Draw a bounding box around every leukocyte (white blood cell).
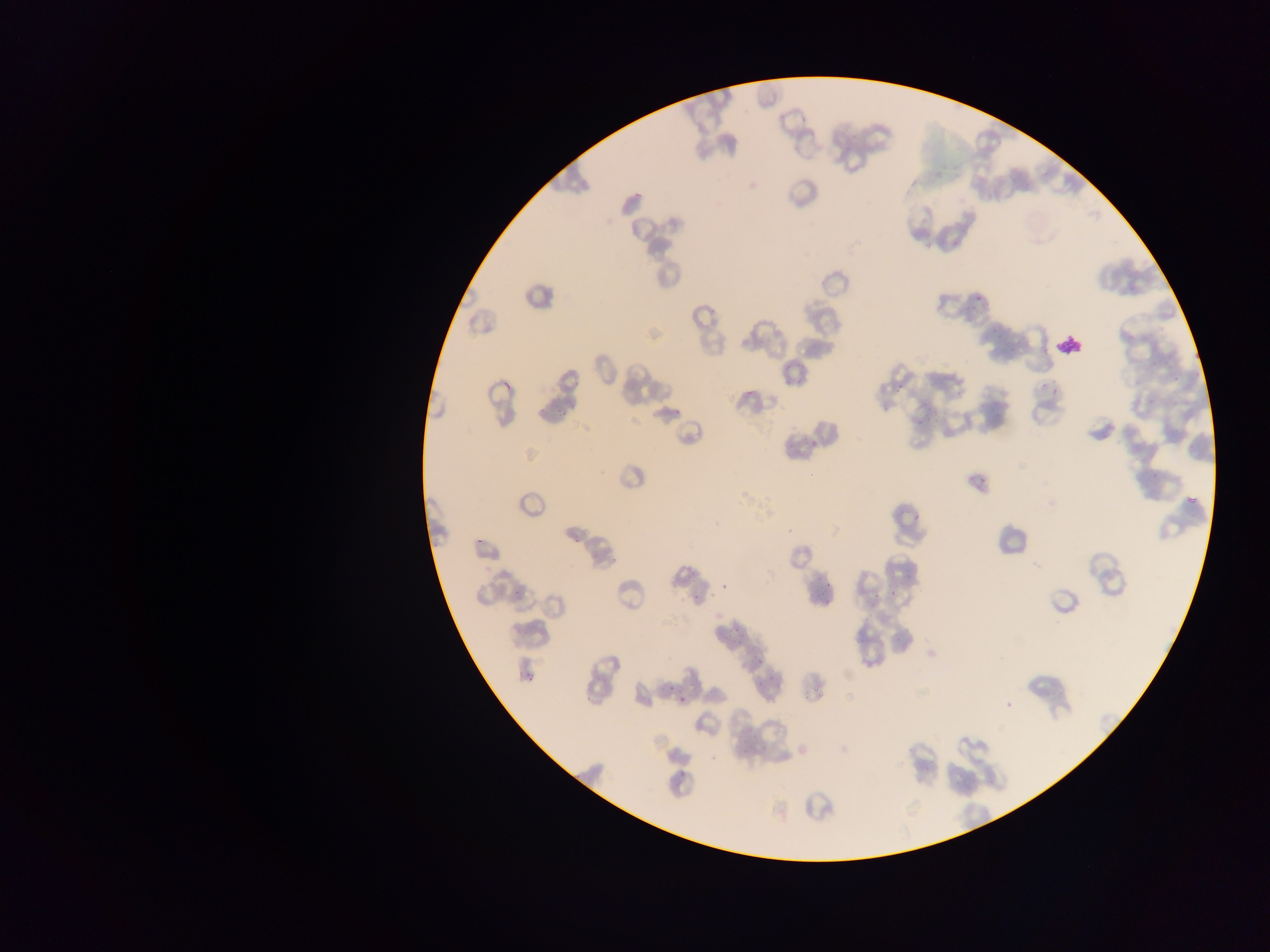
No leukocytes observed.

Approximate bounding boxes as (left, top, right, bottom) in pixels.
Summary:
  - Artifact (stain precipitate or debris) locations: (1058, 327, 1091, 359)
  - Plasmodium parasite locations: (630, 187, 648, 200), (963, 295, 982, 315), (992, 322, 1005, 335), (1043, 336, 1052, 355), (783, 373, 798, 388), (497, 378, 510, 388), (572, 381, 582, 386), (891, 382, 908, 392), (746, 384, 763, 397), (1052, 392, 1062, 397), (554, 395, 571, 418), (672, 407, 680, 416), (879, 408, 895, 415), (912, 415, 928, 428), (806, 441, 818, 452), (976, 473, 986, 484), (1183, 496, 1199, 503), (909, 509, 926, 526), (473, 531, 489, 548), (569, 534, 581, 549), (906, 570, 916, 582), (718, 584, 726, 592), (692, 585, 703, 603), (819, 586, 832, 599), (874, 595, 882, 604), (719, 630, 730, 642), (733, 630, 742, 641), (751, 655, 763, 665), (769, 672, 775, 684), (523, 674, 534, 683), (808, 681, 824, 696), (750, 682, 757, 691), (706, 683, 714, 696), (678, 689, 689, 704), (960, 738, 968, 745), (676, 771, 685, 779), (774, 806, 789, 821) | approximate (x, y) pixel centers of objects too small to bound: (613, 559), (894, 591), (514, 592), (669, 686), (749, 730)
  - Preparation: thin blood smear
  - Image size: 1270×952 pixels
  - Country: Ghana
  - Capture: mobile-phone photograph through a microscope
  - Field of view: single